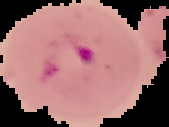 From a thin blood smear. Result: Plasmodium parasites detected. Segmented cell region on a black background. Image is 169×127 pixels.